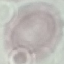
Malaria status: uninfected. Giemsa stain. Acquired by smartphone through the microscope eyepiece. Cell patch, automatically extracted from a larger field of view and resized to 64 × 64 pixels. Thin blood smear.